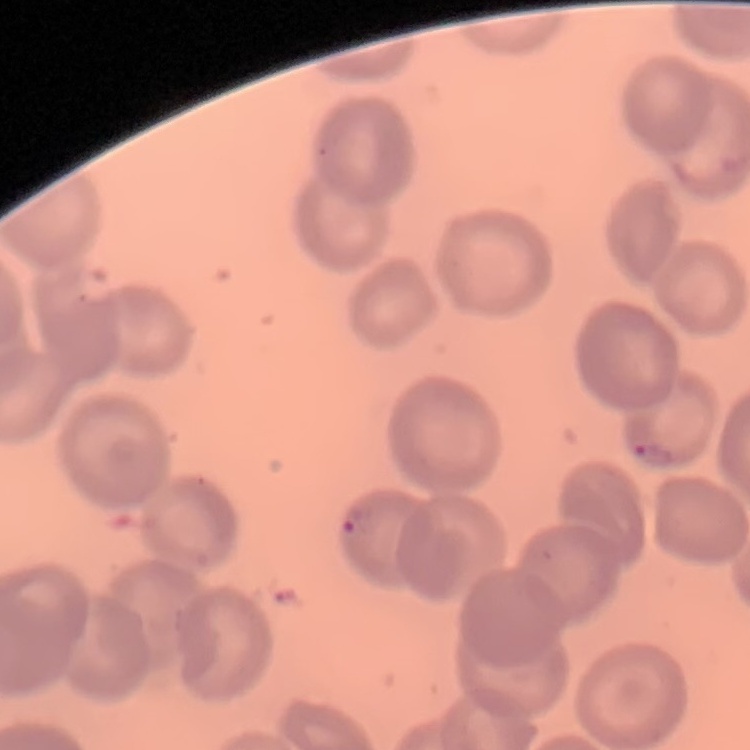

red blood cell morphology = no rouleaux formation
stain = Field's or Giemsa
preparation = thin blood smear
image type = one tile cut from a larger photomicrograph